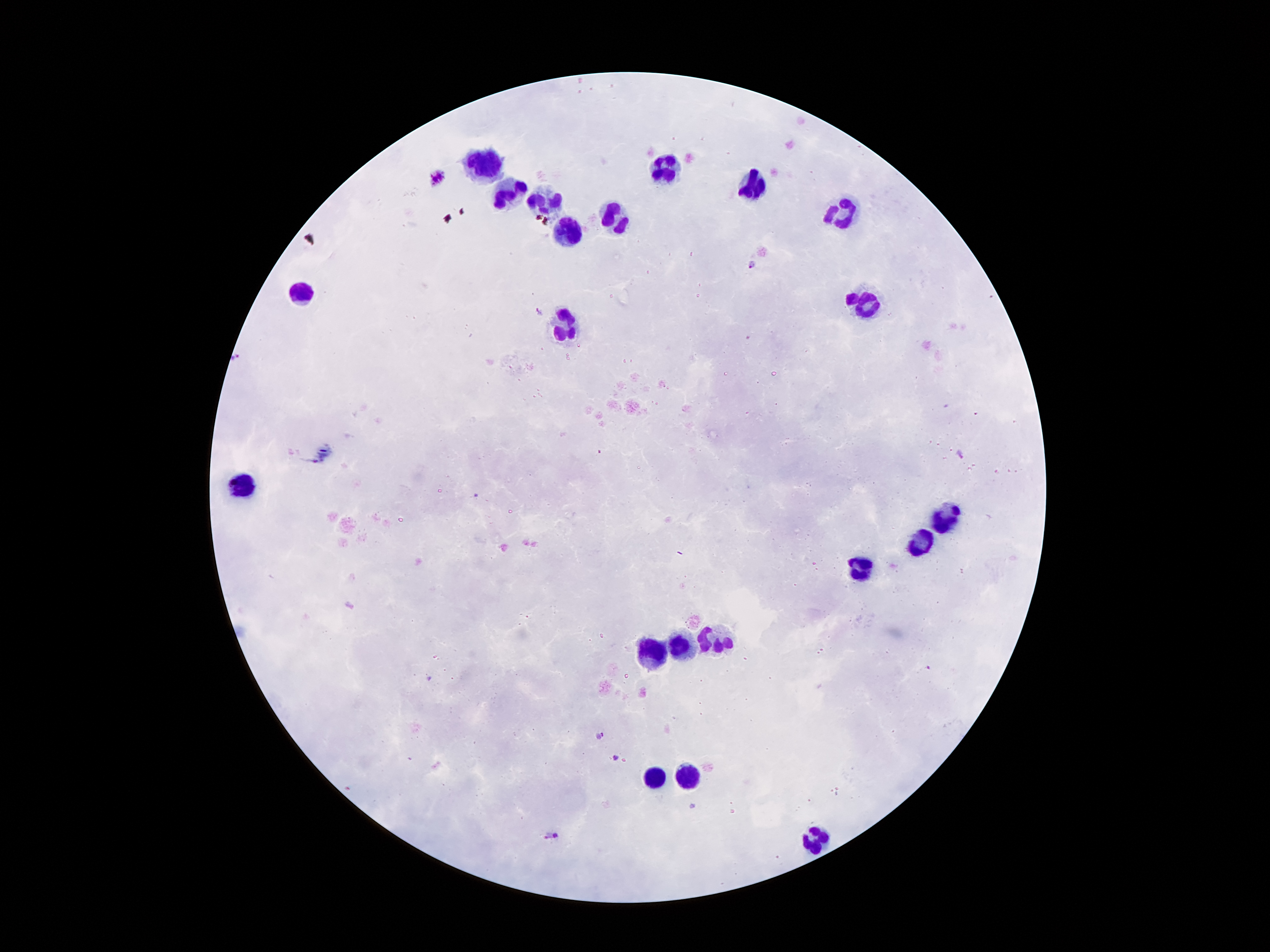 Approximate centers as {x, y} in pixels. Malaria parasite locations: {438, 176}, {751, 264}, {538, 311}, {239, 358}, {962, 455}, {475, 496}, {430, 680}, {599, 735}, {615, 759}, {553, 836}. Leukocyte locations: {484, 163}, {665, 163}, {754, 184}, {509, 195}, {544, 200}, {849, 214}, {612, 217}, {565, 231}, {304, 291}, {864, 306}, {561, 330}, {249, 486}, {944, 519}, {921, 545}, {862, 568}, {714, 640}, {681, 645}, {652, 652}, {687, 775}, {655, 776}, {815, 840}. 100x magnification. Image is 1270×952 pixels. Smartphone photograph taken through the microscope eyepiece. One field from this slide. Thick blood smear. Giemsa-stained preparation. Patient malaria status: infected with Plasmodium falciparum.